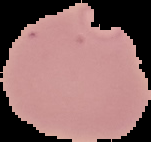

image size = 151×142 pixels
preparation = thin blood film
result = Plasmodium parasites identified
image type = cell region segmented out of the field of view; surrounding area masked to black